Classify this cell by malaria status.
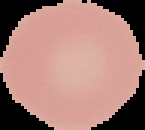

It is uninfected.

preparation = thin blood smear
image size = 145×130 pixels
image type = cell region segmented out of the field of view; surrounding area masked to black